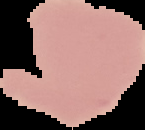
preparation = thin blood smear
image size = 145×130 pixels
image type = segmented cell region on a black background
result = no malaria parasites detected